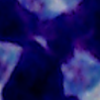

Photomicrograph. 1000x magnification. A leukocyte is seen.